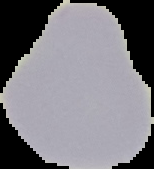
Summary:
  - Malaria status: uninfected
  - Image size: 154×169 pixels
  - Image type: segmented cell region on a black background
  - Preparation: thin blood film